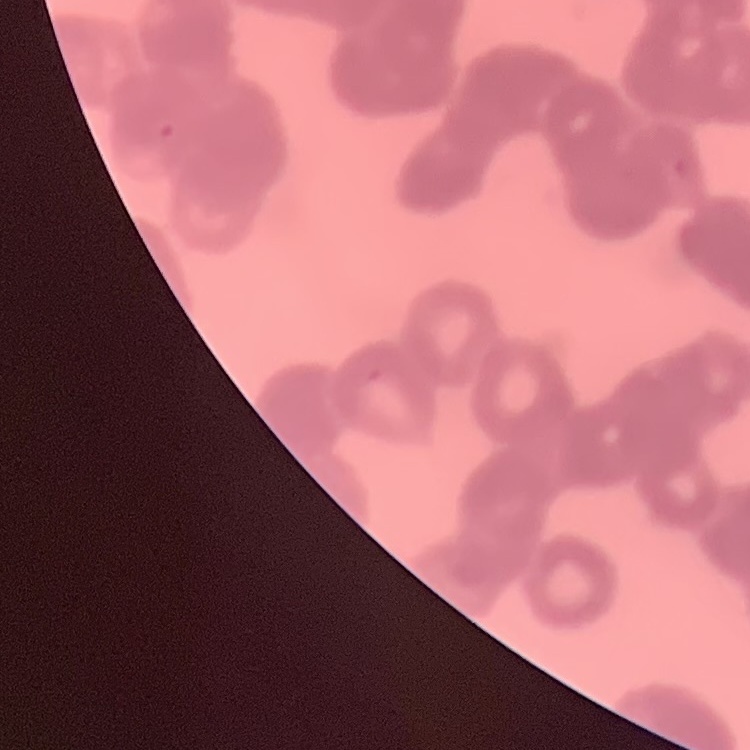 The erythrocytes exhibit rouleaux formation. Thin peripheral smear. Square crop of a larger photomicrograph. Stained with either Field's or Giemsa.